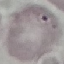
result: negative for malaria parasites
stain: Giemsa
image_type: cell patch, automatically extracted from a larger field of view and resized to 64 × 64 pixels
capture: smartphone through the microscope eyepiece
preparation: thin blood film